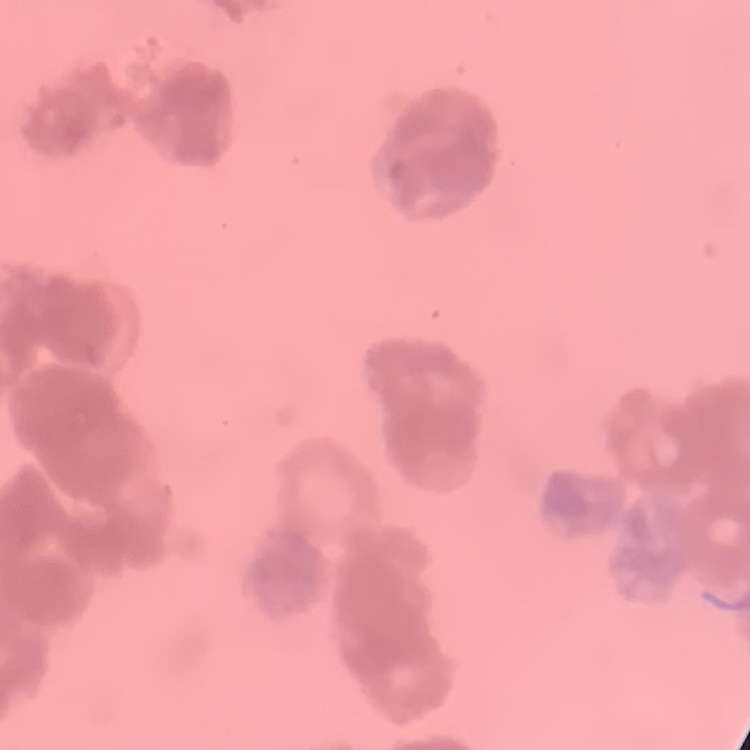
Summary:
  - Red blood cell morphology: rouleaux formation
  - Image type: one tile cut from a larger photomicrograph
  - Stain: Field's or Giemsa
  - Preparation: thin peripheral smear